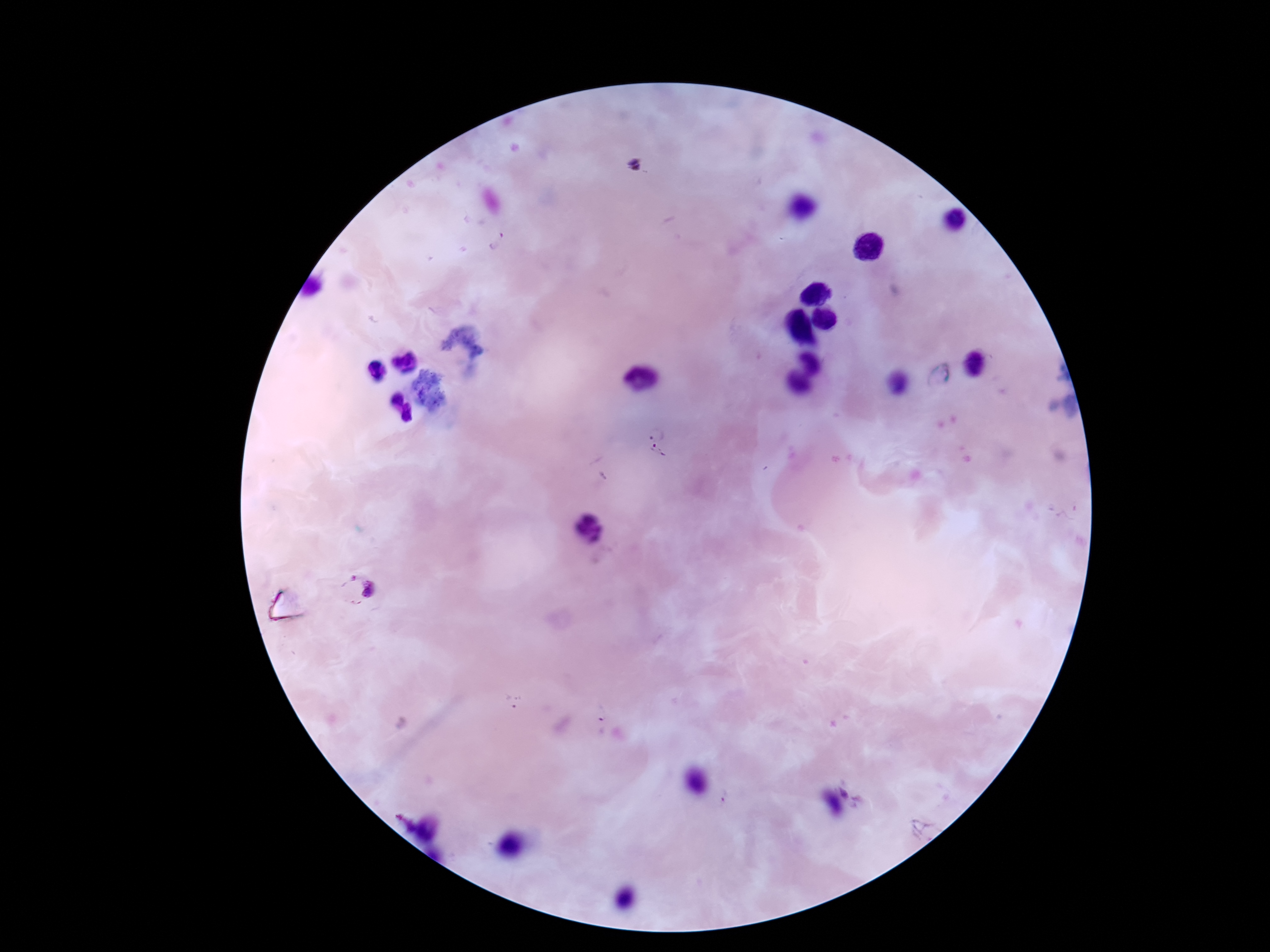

Approximate centers as [x, y] in pixels.
Summary:
  - Plasmodium parasite locations: [635, 165], [497, 242], [656, 434], [658, 453], [356, 589], [515, 701], [602, 713], [857, 793]
  - Magnification: 100x
  - Field of view: single
  - Capture: smartphone camera through the microscope eyepiece
  - Patient malaria status: infected
  - Preparation: thick blood film
  - Stain: Giemsa
  - Image size: 1270×952 pixels